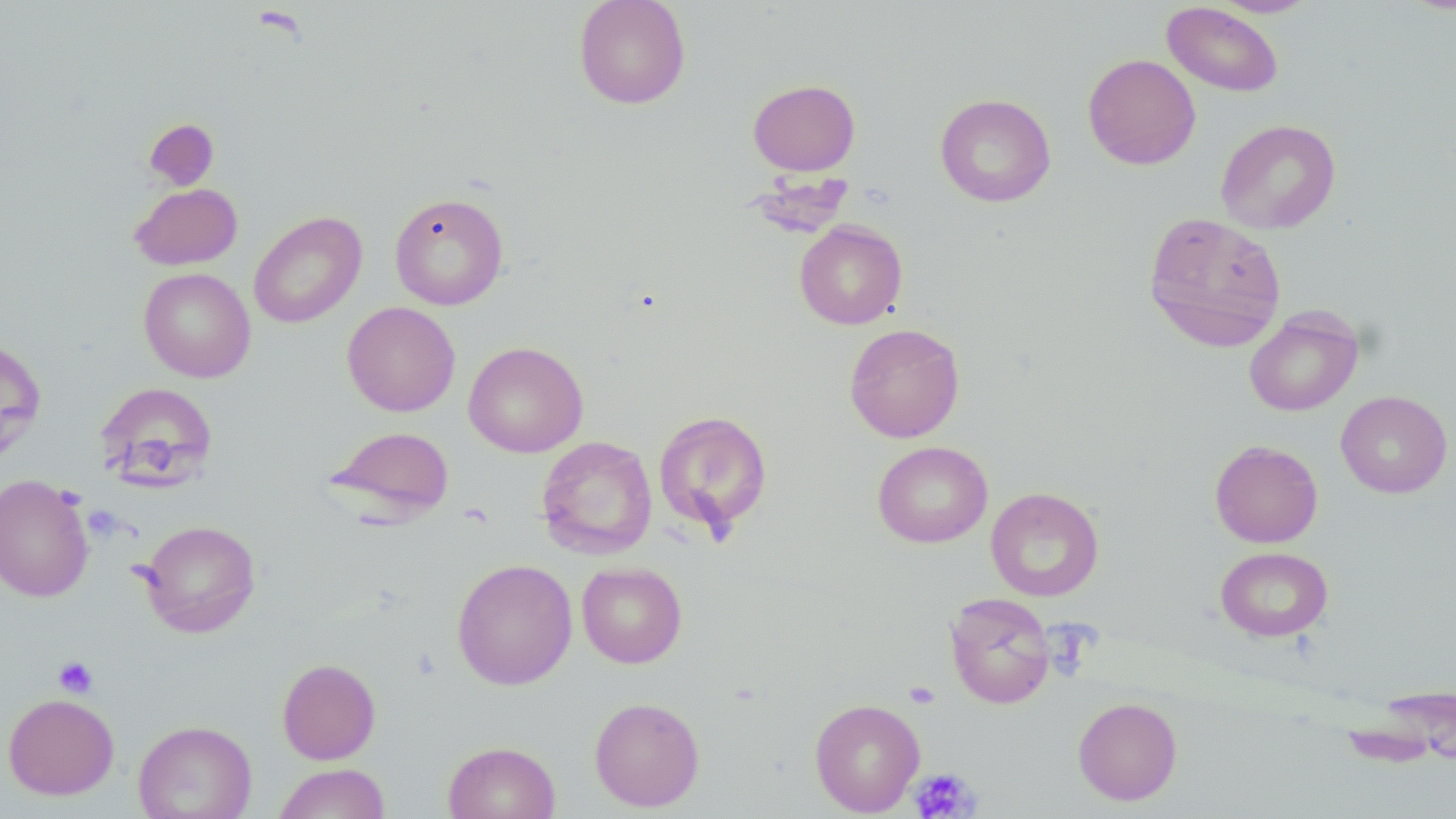

Summary:
  - Coordinate format: approximate bounding boxes as [x1, y1, x2, y2] in pixels
  - Uninfected red blood cell locations (subset): [573, 0, 691, 109], [1210, 0, 1319, 17], [1162, 2, 1284, 97], [1082, 53, 1201, 170], [748, 79, 861, 176], [935, 93, 1056, 207], [1215, 119, 1341, 234], [129, 183, 242, 270], [389, 192, 509, 310], [248, 211, 366, 328], [1143, 211, 1287, 352], [794, 221, 908, 329], [138, 267, 255, 382], [342, 301, 460, 416], [1244, 308, 1363, 416], [844, 323, 965, 443], [0, 338, 46, 467], [463, 341, 588, 458], [94, 382, 218, 489], [1335, 390, 1453, 498], [653, 410, 773, 536], [324, 425, 455, 524], [536, 435, 658, 559], [1209, 440, 1323, 547], [872, 441, 993, 548], [0, 474, 94, 603], [986, 487, 1104, 602], [138, 519, 260, 638], [1215, 546, 1333, 642], [452, 558, 578, 689], [576, 562, 687, 668], [944, 592, 1056, 709], [277, 658, 381, 764], [1361, 682, 1456, 768], [3, 693, 120, 799], [589, 696, 705, 812], [1072, 697, 1182, 805], [809, 698, 925, 815], [133, 719, 257, 818], [442, 741, 560, 819], [273, 763, 391, 818]
  - Platelet locations (subset): [53, 656, 98, 698], [904, 680, 940, 708], [910, 768, 980, 817]
  - Slide-level diagnosis: negative for blood parasites
  - Preparation: thin blood film
  - Image size: 1456×819 pixels
  - Modality: light microscopy
  - Field of view: single
  - Stain: May-Grünwald-Giemsa
  - Magnification: 1000x